Classify this cell by malaria status.
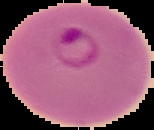

It is parasitized.

Summary:
  - Preparation: thin blood film
  - Image type: segmented cell region on a black background
  - Image size: 154×130 pixels